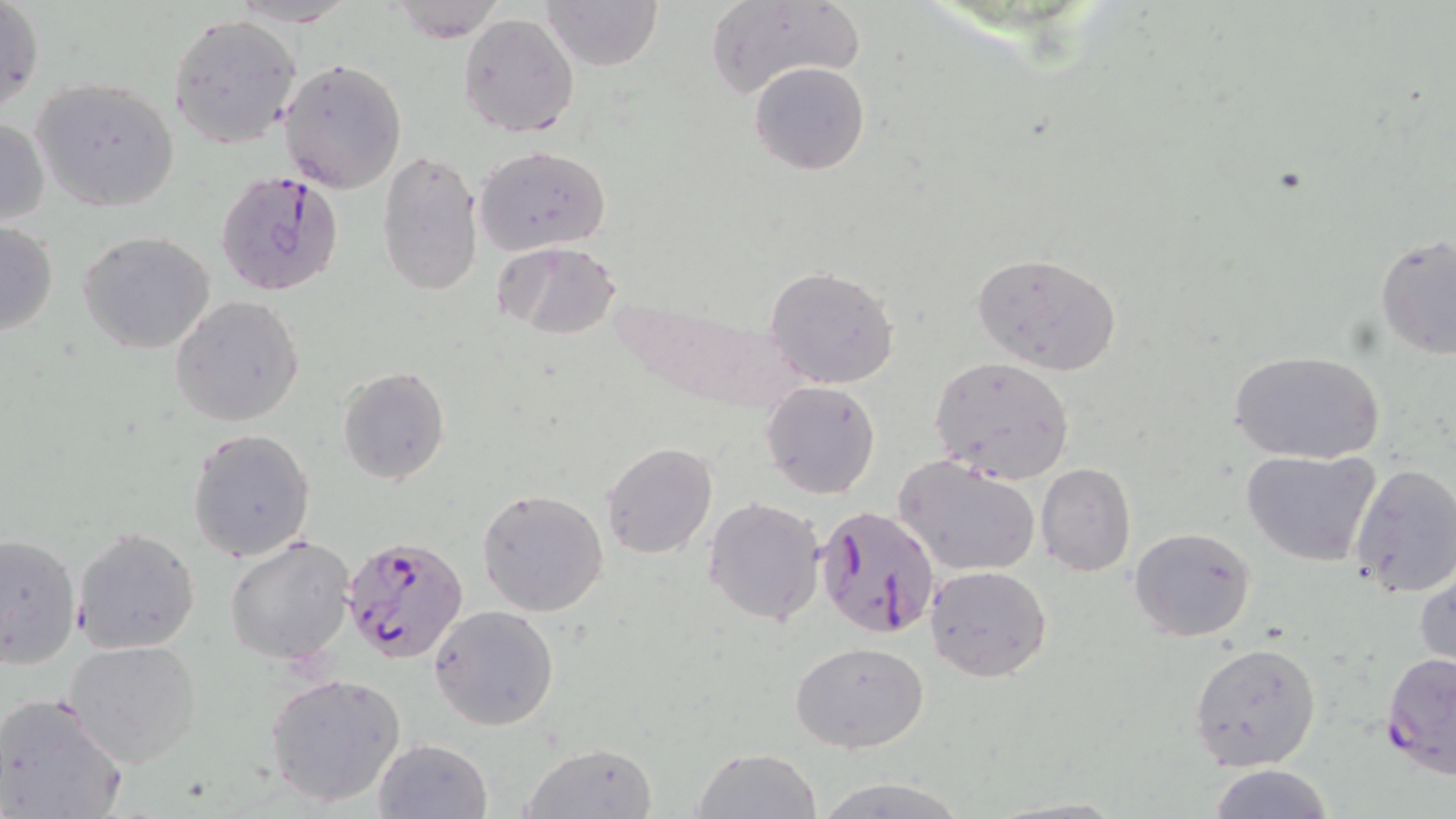

slide-level diagnosis = Plasmodium falciparum
field of view = single
uninfected red blood cell locations = approximate bounding boxes as (x1, y1, x2, y2) in pixels: (1, 0, 43, 114), (390, 0, 504, 43), (541, 0, 665, 70), (230, 1, 354, 26), (704, 2, 864, 100), (459, 12, 579, 137), (169, 14, 302, 147), (280, 58, 406, 193), (749, 62, 871, 176), (32, 78, 180, 211), (0, 115, 49, 227), (474, 145, 610, 253), (376, 148, 483, 295), (1, 219, 58, 339), (78, 231, 217, 355), (1375, 234, 1456, 359), (498, 239, 622, 340), (970, 251, 1121, 376), (763, 267, 899, 389), (171, 295, 306, 427), (1229, 348, 1385, 463), (930, 357, 1076, 486), (337, 366, 451, 484), (762, 381, 882, 499), (186, 427, 314, 562), (601, 441, 717, 560), (1242, 448, 1383, 569), (895, 456, 1041, 578), (1348, 461, 1456, 598), (1035, 464, 1136, 577), (476, 487, 609, 617), (703, 496, 825, 627), (71, 526, 200, 654), (1129, 526, 1257, 642), (0, 533, 81, 669), (225, 534, 355, 667), (1416, 560, 1455, 672), (926, 564, 1051, 680), (430, 604, 560, 730), (64, 639, 201, 767), (790, 642, 930, 752), (1188, 642, 1322, 772), (265, 672, 407, 808), (0, 691, 128, 819), (372, 738, 493, 819), (518, 742, 658, 819), (693, 747, 822, 818), (1207, 765, 1333, 819), (814, 775, 971, 818)
Plasmodium falciparum-infected red blood cell locations = approximate bounding boxes as (x1, y1, x2, y2) in pixels: (216, 171, 346, 297), (815, 508, 939, 640), (342, 536, 469, 667), (1381, 652, 1456, 779)
stain = May-Grünwald-Giemsa
modality = optical microscopy
image size = 1456×819 pixels
preparation = thin blood film
magnification = 1000x